Assess this cell for malaria.
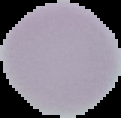
It is uninfected.

Summary:
  - Image size: 121×118 pixels
  - Preparation: thin blood smear
  - Image type: segmented cell region on a black background